Give the position of every malaria parasite and every leukocyte.
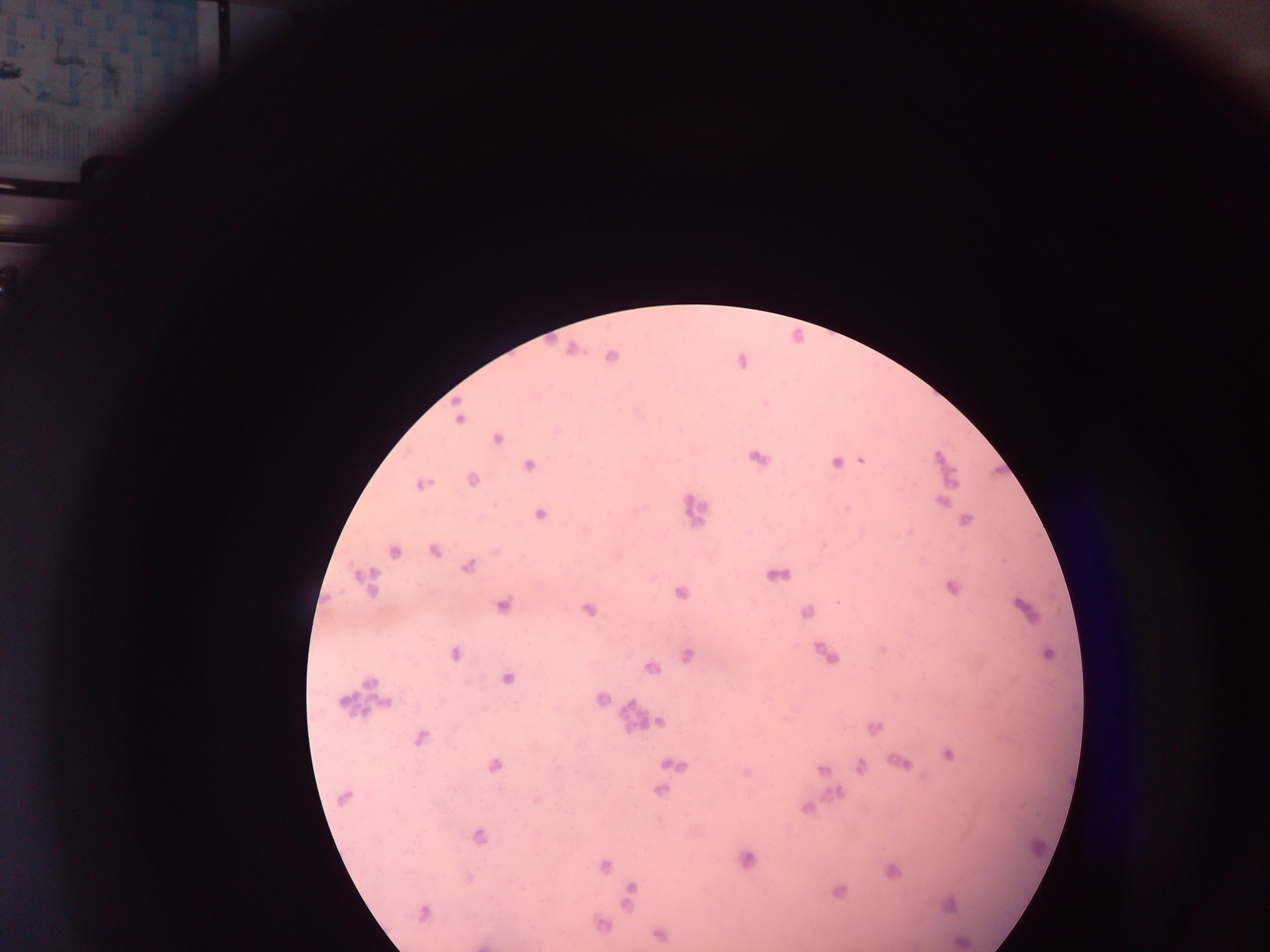

Approximate centers as (x, y) in pixels.
Malaria parasites: (12, 72), (44, 96), (611, 356), (459, 419), (497, 439), (758, 458), (940, 458), (863, 461), (837, 462), (529, 465), (472, 480), (421, 484), (942, 501), (539, 515), (967, 519), (434, 550), (395, 552), (467, 566), (951, 588), (681, 593), (838, 602), (503, 605), (1024, 607), (588, 609), (807, 612), (455, 654), (1048, 654), (688, 655), (651, 668), (506, 678), (370, 682), (601, 698), (344, 700), (386, 703), (660, 722), (875, 728), (420, 738), (948, 754), (902, 763), (495, 766), (673, 766), (860, 766), (823, 770), (661, 790), (344, 798), (536, 800), (806, 808), (479, 837), (748, 859), (605, 865), (893, 872), (839, 891), (950, 905), (423, 912), (661, 936), (960, 942).
Leukocytes (some below the resolvable threshold): (695, 511), (777, 573), (366, 580), (824, 654), (632, 711), (1039, 846).

Photographed through a microscope with a mobile-phone camera. Sample from Ghana. Image is 1270×952 pixels. Thick blood film. Single field of view.